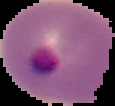

Summary:
  - Image type: segmented cell region on a black background
  - Result: Plasmodium parasites identified
  - Image size: 115×106 pixels
  - Preparation: thin blood film